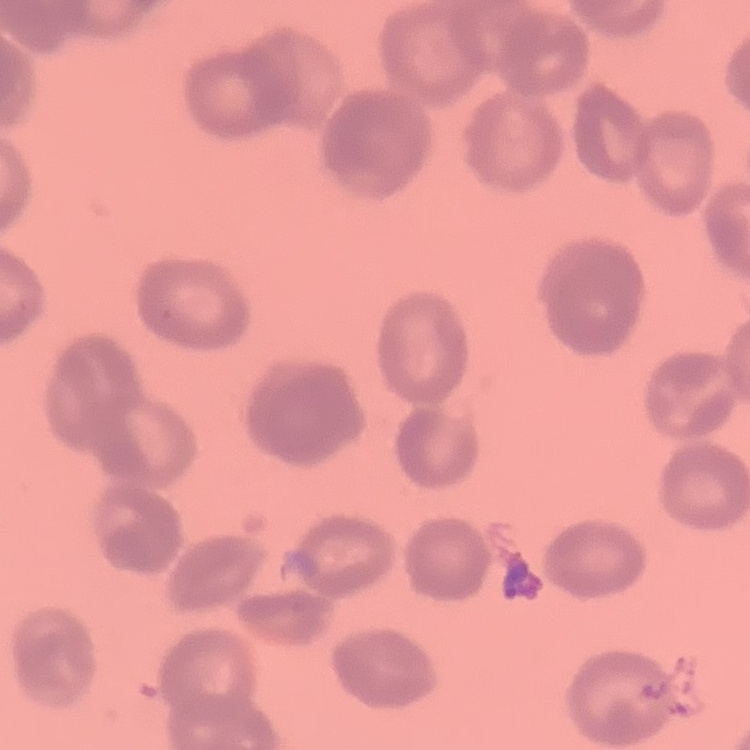

The erythrocytes show rouleaux formation. Thin peripheral smear. Square crop of a larger photomicrograph. Field's or Giemsa stain.